Identify the blood parasite species.
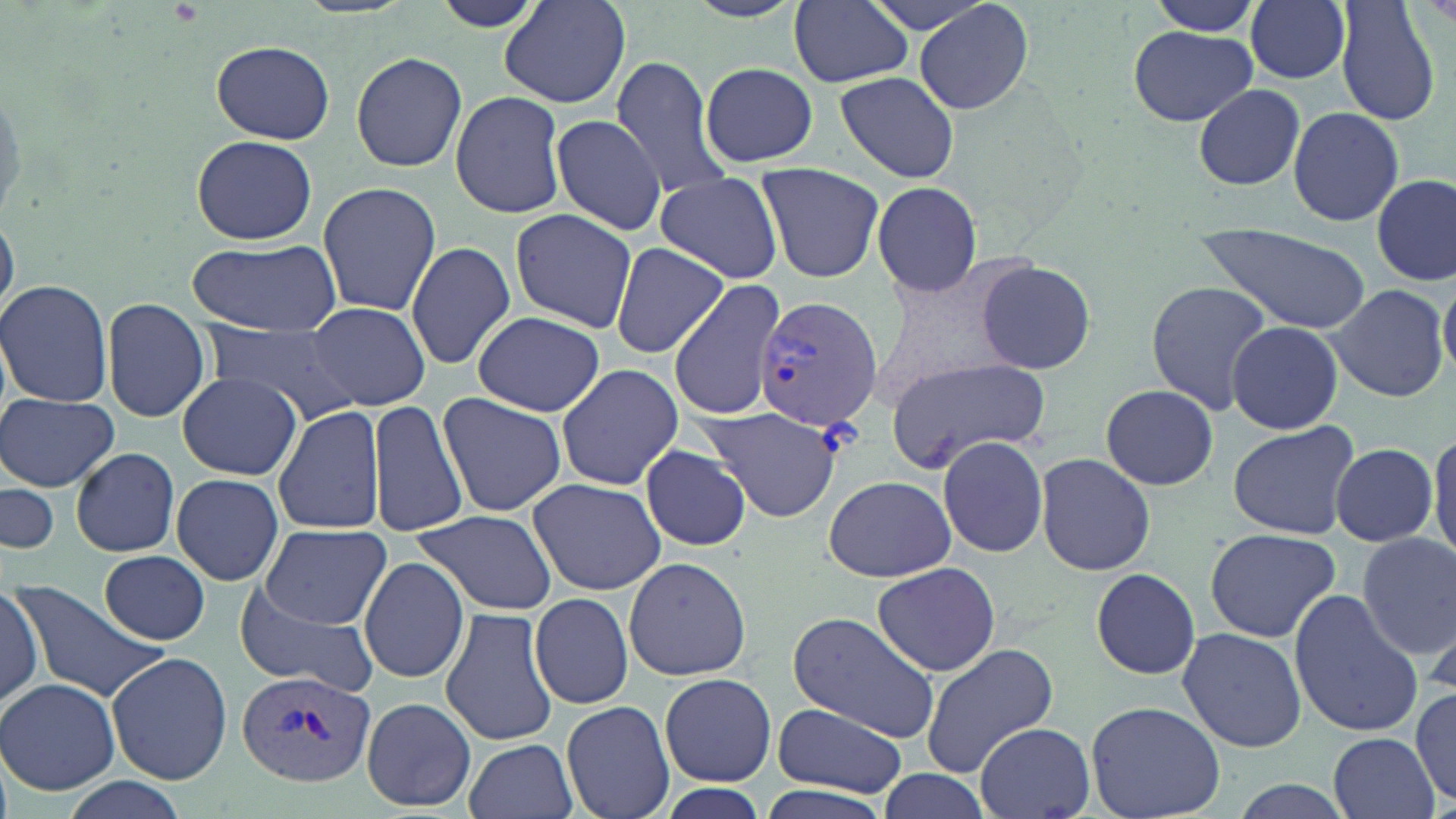
Plasmodium vivax.

Approximate bounding boxes as named x1/y1/x2/y2 corners in pixels. Plasmodium vivax-infected red blood cell locations: (x1=754, y1=292, x2=882, y2=430), (x1=235, y1=668, x2=379, y2=787). Uninfected red blood cell locations: (x1=428, y1=0, x2=549, y2=34), (x1=788, y1=0, x2=914, y2=88), (x1=856, y1=0, x2=1004, y2=35), (x1=914, y1=0, x2=1035, y2=114), (x1=1246, y1=0, x2=1353, y2=84), (x1=1337, y1=0, x2=1444, y2=127), (x1=1143, y1=1, x2=1264, y2=36), (x1=501, y1=3, x2=631, y2=108), (x1=1126, y1=21, x2=1258, y2=128), (x1=212, y1=40, x2=334, y2=143), (x1=350, y1=52, x2=468, y2=172), (x1=609, y1=57, x2=736, y2=202), (x1=698, y1=58, x2=818, y2=169), (x1=834, y1=70, x2=961, y2=183), (x1=1193, y1=83, x2=1305, y2=190), (x1=447, y1=92, x2=568, y2=217), (x1=1288, y1=106, x2=1404, y2=226), (x1=551, y1=112, x2=665, y2=238), (x1=191, y1=135, x2=316, y2=244), (x1=754, y1=163, x2=884, y2=282), (x1=655, y1=175, x2=784, y2=282), (x1=1373, y1=176, x2=1455, y2=286), (x1=315, y1=181, x2=441, y2=319), (x1=869, y1=181, x2=983, y2=296), (x1=0, y1=190, x2=24, y2=335), (x1=510, y1=209, x2=637, y2=332), (x1=1197, y1=225, x2=1372, y2=335), (x1=190, y1=238, x2=342, y2=335), (x1=405, y1=241, x2=515, y2=368), (x1=611, y1=244, x2=731, y2=357), (x1=974, y1=257, x2=1097, y2=376), (x1=1440, y1=274, x2=1456, y2=381), (x1=668, y1=277, x2=787, y2=423), (x1=0, y1=279, x2=114, y2=408), (x1=1145, y1=279, x2=1275, y2=413), (x1=1325, y1=282, x2=1450, y2=403), (x1=101, y1=297, x2=211, y2=423), (x1=305, y1=302, x2=430, y2=411), (x1=473, y1=310, x2=604, y2=417), (x1=1226, y1=320, x2=1344, y2=435), (x1=208, y1=324, x2=359, y2=424), (x1=884, y1=355, x2=1052, y2=473), (x1=555, y1=362, x2=684, y2=492), (x1=177, y1=372, x2=302, y2=480), (x1=1100, y1=385, x2=1218, y2=491), (x1=0, y1=391, x2=119, y2=492), (x1=438, y1=392, x2=567, y2=518), (x1=370, y1=398, x2=468, y2=538), (x1=274, y1=404, x2=387, y2=536), (x1=697, y1=405, x2=844, y2=520), (x1=1227, y1=422, x2=1358, y2=539), (x1=1427, y1=428, x2=1456, y2=559), (x1=937, y1=434, x2=1050, y2=558), (x1=1331, y1=442, x2=1439, y2=547), (x1=640, y1=443, x2=752, y2=552), (x1=71, y1=448, x2=180, y2=557), (x1=1035, y1=453, x2=1156, y2=576), (x1=170, y1=472, x2=285, y2=586), (x1=1, y1=474, x2=60, y2=554), (x1=823, y1=475, x2=955, y2=582), (x1=527, y1=477, x2=665, y2=596), (x1=410, y1=509, x2=558, y2=616), (x1=260, y1=523, x2=390, y2=629), (x1=1204, y1=528, x2=1341, y2=642), (x1=1356, y1=535, x2=1455, y2=660), (x1=99, y1=551, x2=211, y2=644), (x1=623, y1=555, x2=751, y2=681), (x1=359, y1=556, x2=469, y2=683), (x1=871, y1=561, x2=1000, y2=677), (x1=1088, y1=567, x2=1204, y2=680), (x1=20, y1=581, x2=168, y2=698), (x1=232, y1=584, x2=379, y2=696), (x1=0, y1=585, x2=44, y2=711), (x1=1288, y1=590, x2=1425, y2=736), (x1=530, y1=593, x2=635, y2=709), (x1=440, y1=609, x2=557, y2=746), (x1=787, y1=612, x2=940, y2=739), (x1=1177, y1=627, x2=1308, y2=753), (x1=919, y1=643, x2=1059, y2=775), (x1=107, y1=651, x2=232, y2=785), (x1=660, y1=673, x2=775, y2=785), (x1=0, y1=679, x2=121, y2=795), (x1=1411, y1=690, x2=1456, y2=803), (x1=361, y1=696, x2=475, y2=810), (x1=563, y1=700, x2=675, y2=819), (x1=1087, y1=701, x2=1224, y2=819), (x1=770, y1=702, x2=909, y2=800), (x1=974, y1=722, x2=1095, y2=817), (x1=1327, y1=731, x2=1439, y2=819), (x1=464, y1=738, x2=578, y2=819), (x1=875, y1=769, x2=993, y2=819), (x1=1223, y1=778, x2=1357, y2=819), (x1=60, y1=780, x2=188, y2=817), (x1=653, y1=780, x2=772, y2=819), (x1=749, y1=781, x2=904, y2=819). Image is 1456×819 pixels. Thin blood smear. 1000x magnification. Single field of view. Optical microscopy. May-Grünwald-Giemsa-stained preparation.